Locate every uninfected red blood cell.
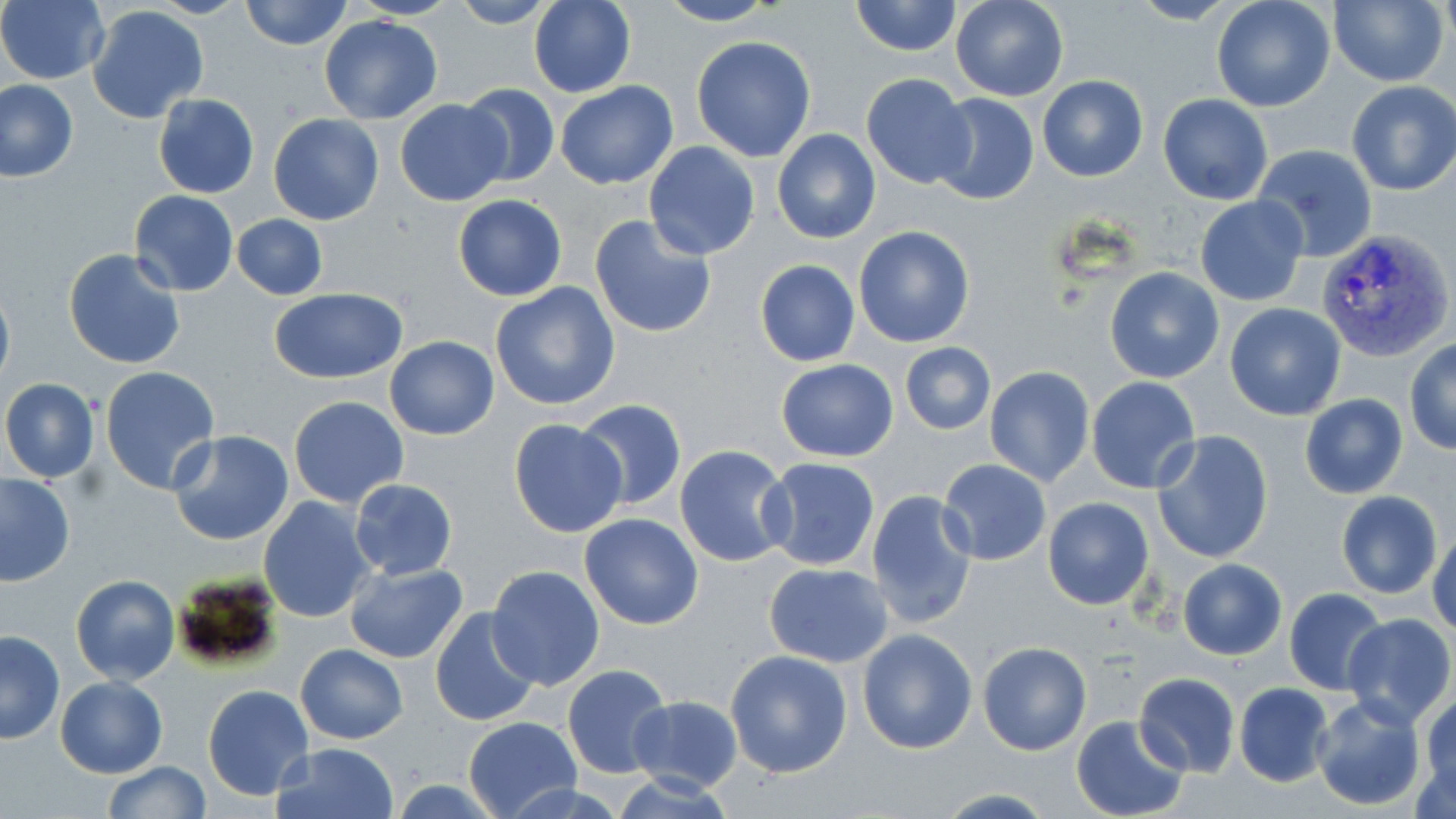
Approximate bounding boxes as (x1, y1, x2, y2) in pixels.
Uninfected red blood cells: (146, 0, 248, 18), (239, 0, 352, 51), (351, 0, 459, 20), (447, 0, 557, 29), (528, 0, 635, 98), (950, 0, 1069, 102), (1127, 0, 1240, 25), (1210, 0, 1336, 113), (1330, 0, 1450, 87), (0, 1, 109, 84), (656, 1, 780, 26), (851, 1, 961, 56), (86, 5, 210, 124), (319, 15, 441, 124), (691, 35, 816, 163), (861, 73, 975, 190), (1038, 75, 1148, 182), (1, 79, 78, 183), (554, 79, 679, 190), (1347, 80, 1456, 196), (458, 84, 561, 189), (153, 93, 258, 199), (929, 93, 1039, 206), (1157, 94, 1272, 204), (394, 100, 510, 206), (267, 113, 384, 225), (772, 129, 880, 244), (644, 140, 760, 259), (1253, 143, 1378, 262), (129, 190, 239, 296), (452, 194, 566, 302), (1194, 195, 1309, 306), (231, 214, 328, 299), (588, 215, 717, 340), (854, 226, 975, 348), (62, 247, 187, 370), (762, 257, 873, 464), (754, 259, 860, 366), (1104, 266, 1225, 383), (0, 277, 15, 394), (490, 283, 621, 412), (268, 288, 409, 382), (1224, 302, 1347, 421), (385, 337, 499, 439), (1405, 339, 1456, 454), (900, 342, 996, 435), (777, 358, 899, 463), (984, 366, 1095, 488), (99, 367, 220, 495), (1086, 377, 1200, 495), (1, 378, 100, 484), (1300, 393, 1408, 498), (289, 396, 409, 508), (574, 399, 687, 512), (508, 419, 629, 538), (169, 429, 294, 547), (1153, 430, 1274, 563), (675, 445, 796, 568), (760, 457, 883, 571), (938, 457, 1053, 565), (0, 473, 74, 587), (350, 478, 457, 581), (1336, 490, 1442, 598), (867, 491, 979, 629), (259, 496, 376, 624), (1041, 496, 1155, 610), (579, 513, 704, 630), (1428, 527, 1456, 638), (1178, 559, 1286, 659), (345, 562, 469, 665), (763, 562, 893, 667), (487, 564, 605, 690), (72, 574, 179, 685), (1283, 588, 1388, 696), (429, 607, 542, 729), (1341, 613, 1455, 728), (857, 629, 977, 754), (1, 631, 65, 744), (977, 642, 1091, 755), (295, 643, 407, 745), (725, 649, 852, 778), (563, 663, 671, 778), (1134, 672, 1240, 776), (56, 676, 166, 777), (1234, 683, 1335, 786), (203, 684, 315, 800), (1421, 691, 1456, 805), (628, 694, 744, 793), (1310, 694, 1428, 812), (1071, 715, 1190, 819), (463, 716, 579, 819), (273, 741, 399, 819), (104, 760, 211, 817), (391, 778, 507, 817), (934, 788, 1060, 817).

{
  "slide_level_diagnosis": "Plasmodium vivax",
  "magnification": "1000x",
  "plasmodium_vivax_infected_red_blood_cell_locations": "approximate bounding boxes as (x1, y1, x2, y2) in pixels: (1317, 228, 1453, 363)",
  "stain": "May-Grünwald-Giemsa",
  "preparation": "thin blood smear",
  "field_of_view": "one of a larger specimen",
  "image_size": "1456×819 pixels",
  "modality": "optical microscopy"
}